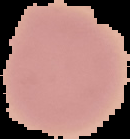
image size = 130×139 pixels
preparation = thin blood smear
malaria status = uninfected
image type = segmented cell region on a black background